Assess for parasitized red blood cells.
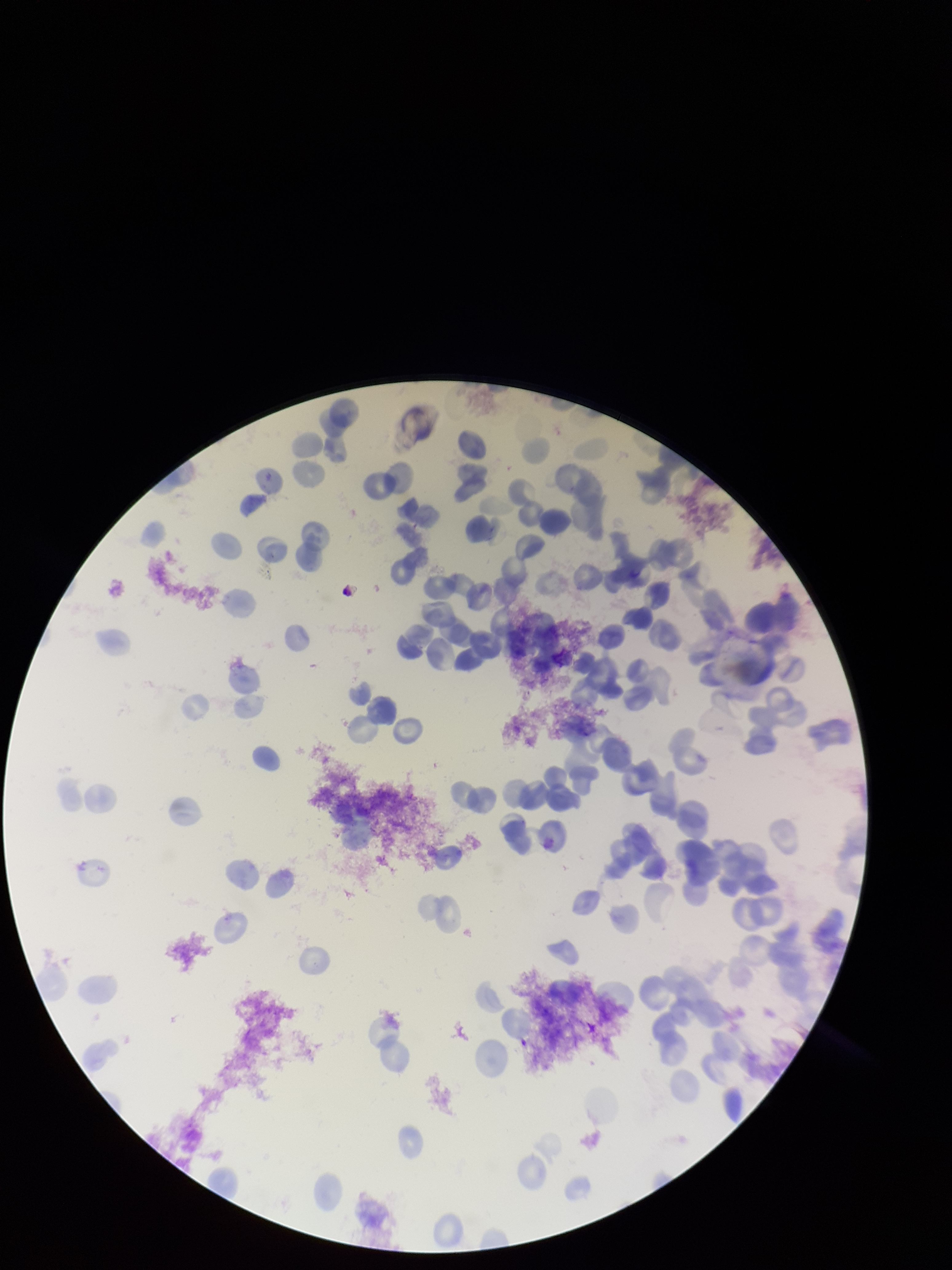

None seen.

Summary:
  - Preparation: thin blood smear
  - Stain: Giemsa
  - Field of view: single
  - Species reported for this patient: Plasmodium vivax
  - Image size: 952×1270 pixels
  - Parasitized red blood cell count: 0
  - Capture: smartphone photograph through the microscope eyepiece
  - Red blood cell count: 117
  - Patient malaria status: infected